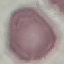 Result: no malaria parasites seen. Thin smear of blood. Cell patch, automatically extracted from a larger field of view and resized to 64 × 64 pixels. Acquired by smartphone through the microscope eyepiece. Giemsa-stained preparation.